Report the malaria status of this cell.
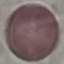
It is uninfected.

Giemsa stain. Thin blood film. Photographed with a smartphone camera at the microscope eyepiece. Cell patch, automatically extracted from a larger field of view and resized to 64 × 64 pixels.